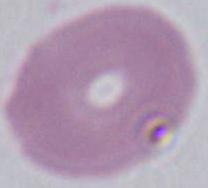

identification = erythrocyte
magnification = 1000x
modality = photomicrograph